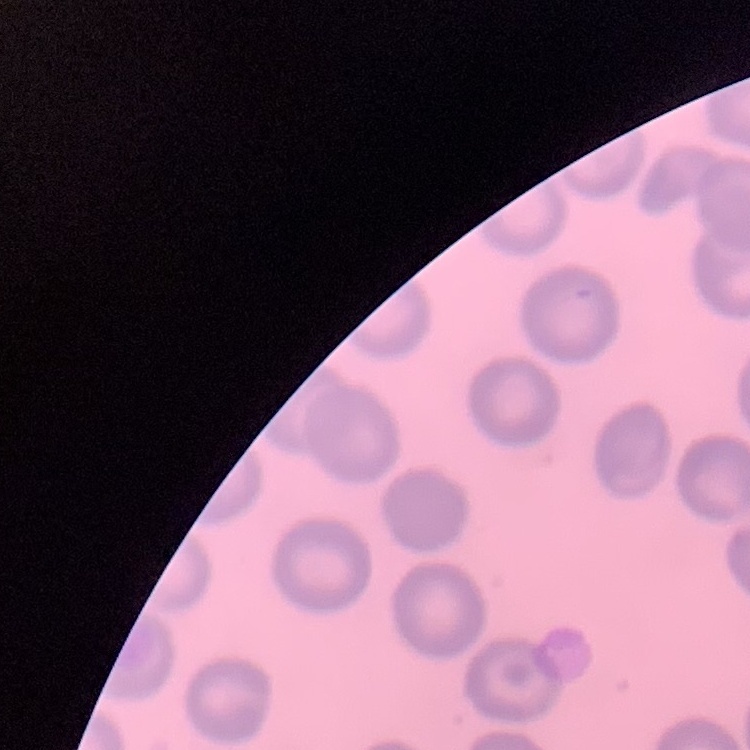
Summary:
  - Red blood cell morphology: no rouleaux formation
  - Stain: Field's or Giemsa
  - Image type: one tile cut from a larger photomicrograph
  - Preparation: thin blood film